Report the malaria status of this cell.
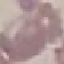

Uninfected.

image type = automatically extracted cell patch, resized to 64 × 64 pixels
stain = Giemsa
preparation = thin blood film
capture = smartphone camera at the microscope eyepiece